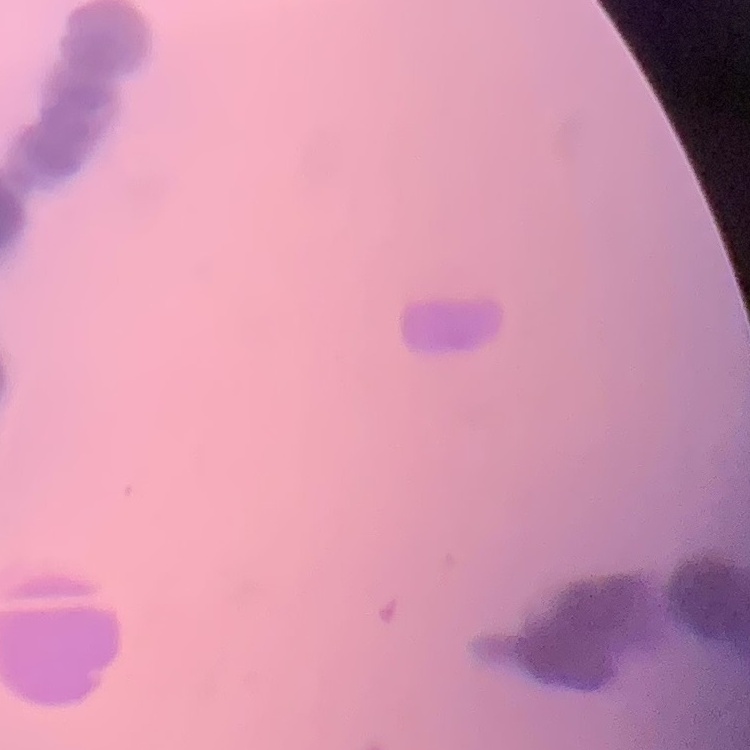

{
  "red_blood_cell_morphology": "rouleaux formation",
  "preparation": "thin blood smear",
  "image_type": "one tile cut from a larger photomicrograph",
  "stain": "Field's or Giemsa"
}